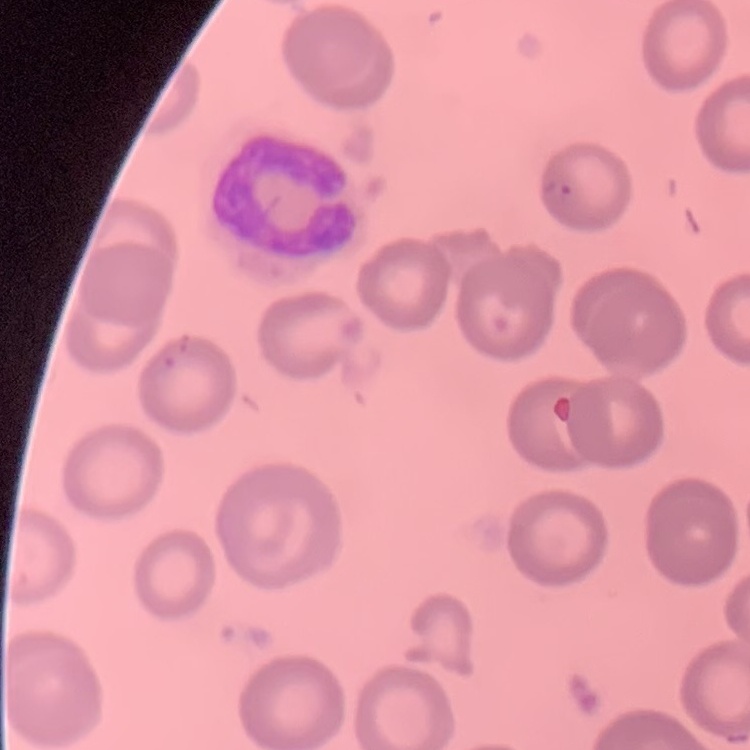

Summary:
  - Erythrocyte morphology: no rouleaux formation
  - Preparation: thin blood film
  - Stain: Field's or Giemsa
  - Image type: square crop of a larger photomicrograph